Outline each blood parasite and name the species.
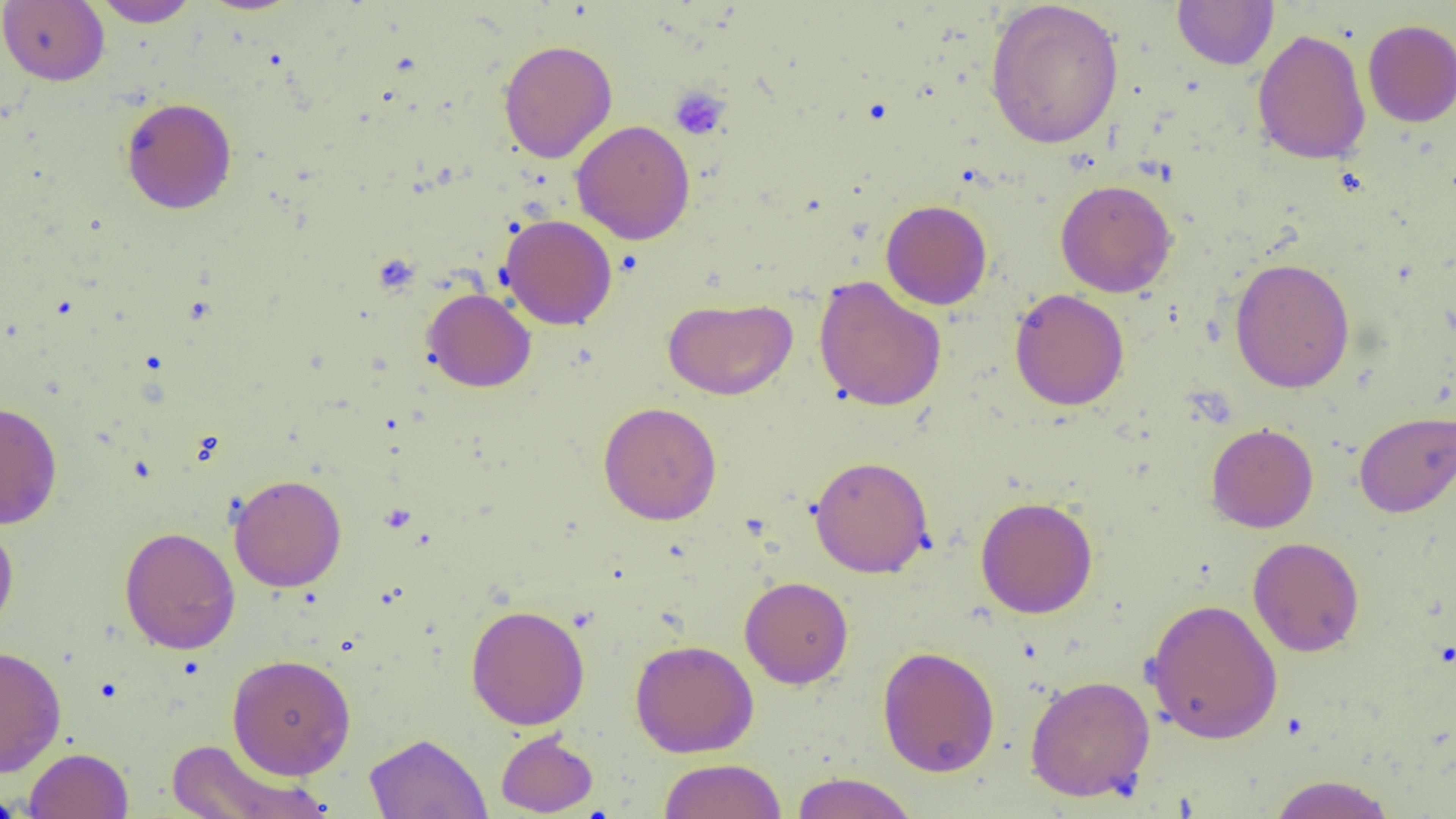

No blood parasites seen.

{
  "slide_level_diagnosis": "no evidence of blood parasites",
  "field_of_view": "one of a larger specimen",
  "platelet_locations": "approximate bounding boxes as (x1,y1)-(x2,y2) corner pairs in pixels: (669,86)-(730,140)",
  "preparation": "thin blood smear",
  "image_size": "1456×819 pixels",
  "uninfected_red_blood_cell_locations": "approximate bounding boxes as (x1,y1)-(x2,y2) corner pairs in pixels: (0,0)-(109,86), (91,0)-(200,27), (1172,0)-(1279,70), (984,1)-(1125,150), (1362,19)-(1456,127), (1252,28)-(1372,166), (497,39)-(617,163), (120,96)-(237,214), (571,119)-(696,245), (1055,179)-(1177,297), (881,200)-(992,309), (499,213)-(617,330), (1229,257)-(1355,393), (813,276)-(947,412), (422,287)-(536,392), (1010,288)-(1130,410), (663,297)-(797,400), (0,401)-(63,529), (598,401)-(722,525), (1353,410)-(1456,518), (1205,422)-(1319,533), (809,455)-(934,578), (228,474)-(347,592), (975,496)-(1098,618), (0,514)-(19,640), (119,526)-(240,655), (1248,537)-(1364,657), (740,575)-(854,689), (1144,598)-(1284,745), (465,604)-(590,729), (630,639)-(759,758), (0,644)-(67,777), (877,645)-(1000,777), (227,653)-(356,780), (1024,674)-(1155,803), (495,730)-(598,817), (364,732)-(492,819), (164,739)-(330,819), (24,747)-(134,819), (656,758)-(787,819), (790,772)-(919,818), (1266,774)-(1398,819), (0,788)-(36,818)",
  "modality": "optical microscopy",
  "magnification": "1000x"
}